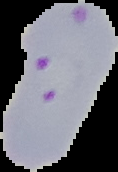

Summary:
  - Image size: 118×172 pixels
  - Preparation: thin blood smear
  - Malaria status: parasitized
  - Image type: cell region segmented out of the field of view; surrounding area masked to black